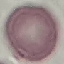

Summary:
  - Result: no malaria parasites detected
  - Stain: Giemsa
  - Image type: cell patch, automatically extracted from a larger field of view and resized to 64 × 64 pixels
  - Preparation: thin smear
  - Capture: smartphone through the microscope eyepiece